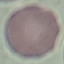

Summary:
  - Malaria status: uninfected
  - Preparation: thin blood film
  - Image type: automatically extracted cell patch, resized to 64 × 64 pixels
  - Capture: smartphone through the microscope eyepiece
  - Stain: Giemsa